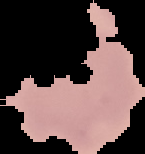
Image is 145×154 pixels. From a thin blood film. Malaria status: uninfected. Cell region segmented out of the field of view; the surrounding area is masked to black.